Assess this cell for malaria.
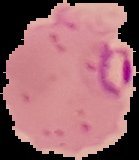
Parasitized.

From a thin blood film. The area outside the segmented cell region is set to black. Image is 139×160 pixels.